Locate every Babesia divergens-infected red blood cell.
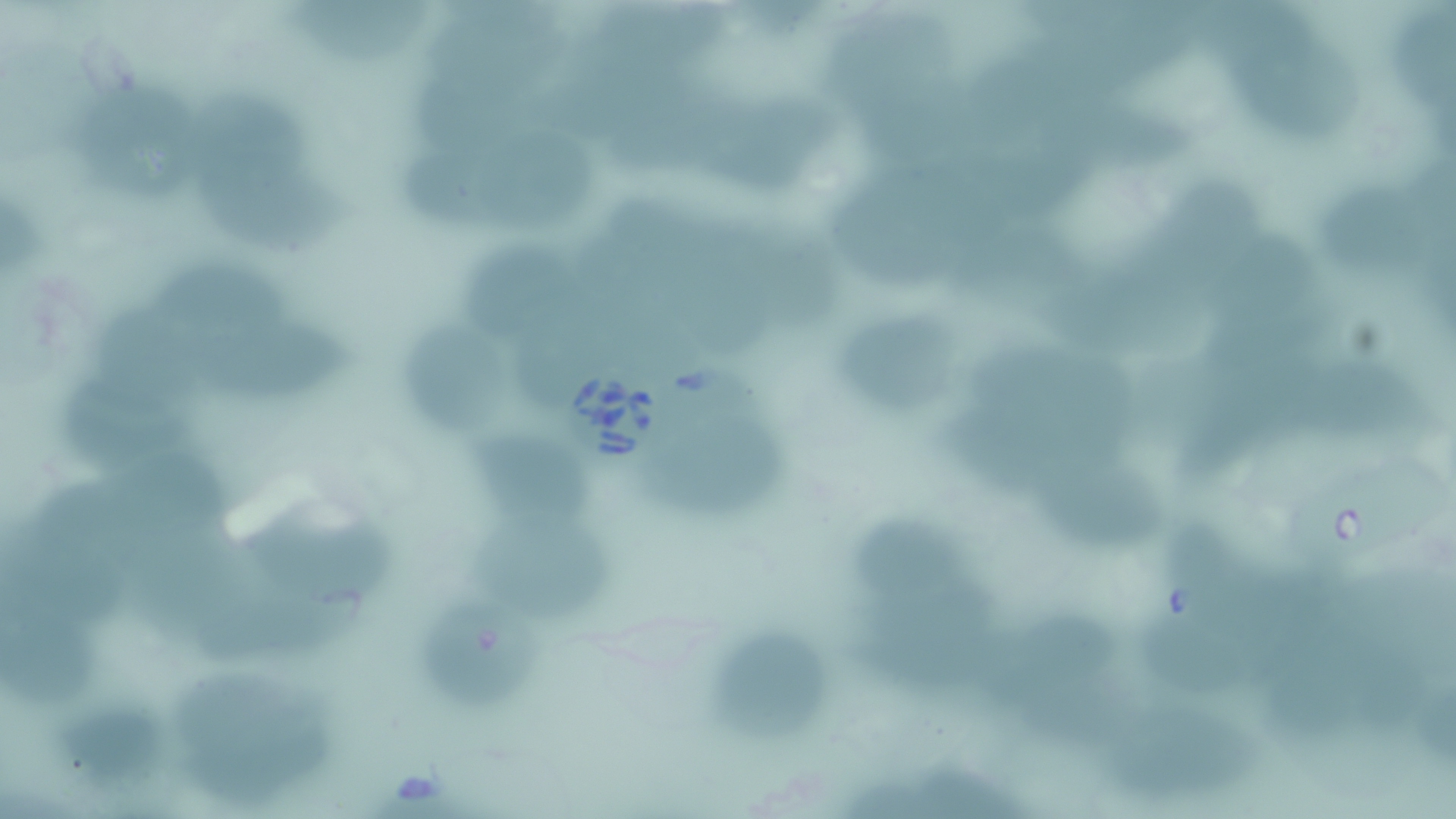
Approximate bounding boxes as named x1/y1/x2/y2 corners in pixels.
Babesia divergens-infected red blood cells: (x1=562, y1=368, x2=674, y2=477), (x1=1275, y1=454, x2=1451, y2=565).

slide-level diagnosis = Babesia divergens
field of view = one of a larger specimen
uninfected red blood cell locations = approximate bounding boxes as named x1/y1/x2/y2 corners in pixels: (x1=290, y1=3, x2=433, y2=66), (x1=605, y1=3, x2=739, y2=77), (x1=1396, y1=6, x2=1453, y2=123), (x1=828, y1=7, x2=963, y2=116), (x1=1249, y1=31, x2=1373, y2=148), (x1=550, y1=65, x2=690, y2=132), (x1=74, y1=76, x2=200, y2=183), (x1=425, y1=82, x2=574, y2=151), (x1=615, y1=88, x2=737, y2=172), (x1=724, y1=98, x2=842, y2=198), (x1=197, y1=100, x2=324, y2=192), (x1=875, y1=101, x2=979, y2=170), (x1=1066, y1=112, x2=1205, y2=180), (x1=399, y1=136, x2=509, y2=226), (x1=496, y1=137, x2=601, y2=235), (x1=975, y1=151, x2=1093, y2=219), (x1=1170, y1=175, x2=1272, y2=270), (x1=217, y1=180, x2=361, y2=263), (x1=845, y1=185, x2=977, y2=296), (x1=1337, y1=199, x2=1430, y2=278), (x1=692, y1=219, x2=788, y2=373), (x1=774, y1=220, x2=847, y2=317), (x1=1217, y1=235, x2=1337, y2=309), (x1=454, y1=239, x2=563, y2=332), (x1=967, y1=247, x2=1091, y2=317), (x1=145, y1=253, x2=303, y2=340), (x1=1071, y1=278, x2=1212, y2=351), (x1=84, y1=306, x2=228, y2=393), (x1=849, y1=317, x2=961, y2=410), (x1=418, y1=326, x2=513, y2=430), (x1=969, y1=326, x2=1118, y2=423), (x1=202, y1=333, x2=365, y2=408), (x1=1312, y1=360, x2=1432, y2=419), (x1=64, y1=364, x2=185, y2=444), (x1=1185, y1=381, x2=1318, y2=489), (x1=952, y1=416, x2=1079, y2=494), (x1=475, y1=430, x2=601, y2=523), (x1=666, y1=436, x2=798, y2=546), (x1=100, y1=442, x2=237, y2=549), (x1=23, y1=471, x2=153, y2=574), (x1=1046, y1=476, x2=1182, y2=558), (x1=263, y1=486, x2=408, y2=589), (x1=479, y1=514, x2=622, y2=623), (x1=863, y1=523, x2=971, y2=615), (x1=1181, y1=528, x2=1317, y2=613), (x1=154, y1=543, x2=271, y2=644), (x1=0, y1=576, x2=111, y2=717), (x1=217, y1=577, x2=375, y2=662), (x1=422, y1=601, x2=554, y2=711), (x1=1259, y1=605, x2=1385, y2=749), (x1=857, y1=606, x2=1001, y2=688), (x1=1001, y1=609, x2=1130, y2=694), (x1=1157, y1=615, x2=1268, y2=695), (x1=715, y1=639, x2=842, y2=738), (x1=1357, y1=651, x2=1433, y2=750), (x1=184, y1=666, x2=327, y2=786), (x1=1097, y1=706, x2=1271, y2=801)
modality = optical microscopy
magnification = 1000x
stain = May-Grünwald-Giemsa
preparation = thin blood smear
image size = 1456×819 pixels